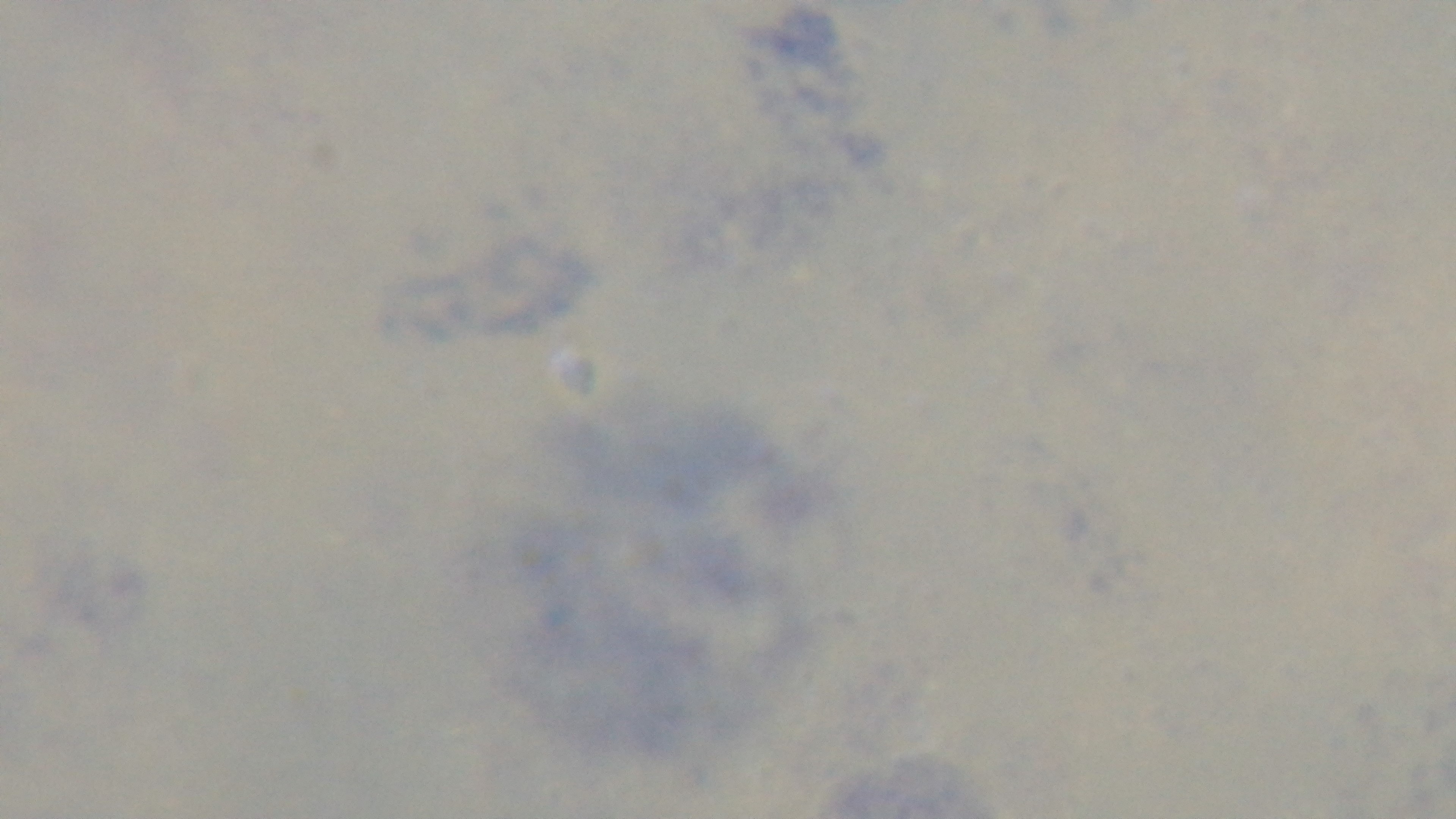
Summary:
  - Field of view: one from the slide
  - Capture: mounted 4K digital camera
  - Malaria status: negative
  - Stain: Giemsa
  - Preparation: thick
  - Modality: light microscopy
  - Objective: 100x oil immersion